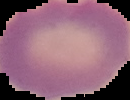
Summary:
  - Image type: segmented cell region on a black background
  - Malaria status: uninfected
  - Image size: 130×100 pixels
  - Preparation: thin blood smear